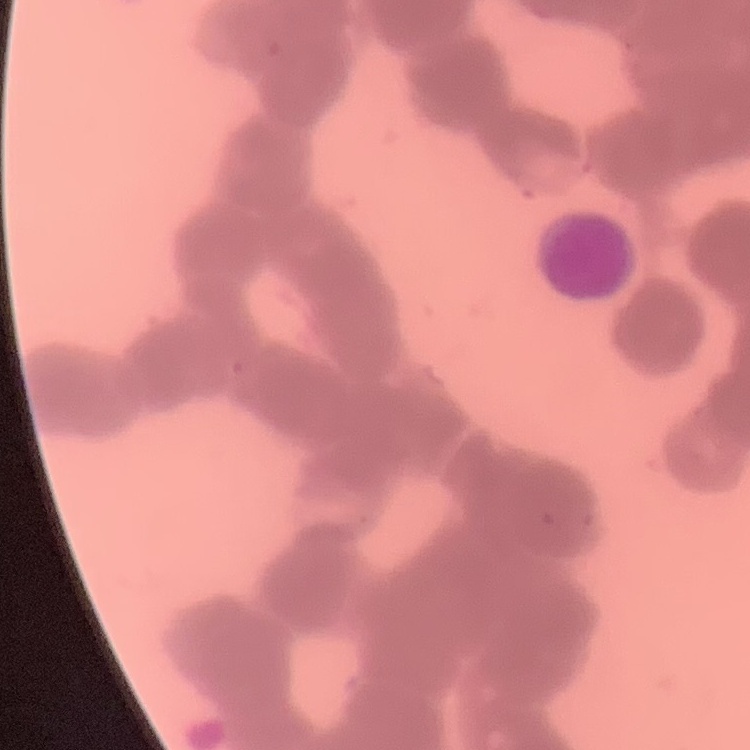
Summary:
  - Red blood cell morphology: rouleaux formation
  - Image type: one tile cut from a larger photomicrograph
  - Preparation: thin blood smear
  - Stain: Field's or Giemsa